Classify this cell by malaria status.
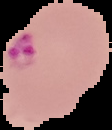
It is parasitized.

{
  "image_size": "112×130 pixels",
  "preparation": "thin blood film",
  "image_type": "segmented cell region on a black background"
}